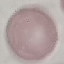
Result: no malaria parasites seen. Acquired by smartphone through the microscope eyepiece. Cell patch, automatically extracted from a larger field of view and resized to 64 × 64 pixels. Thin blood film. Giemsa-stained preparation.